Locate every Plasmodium parasite.
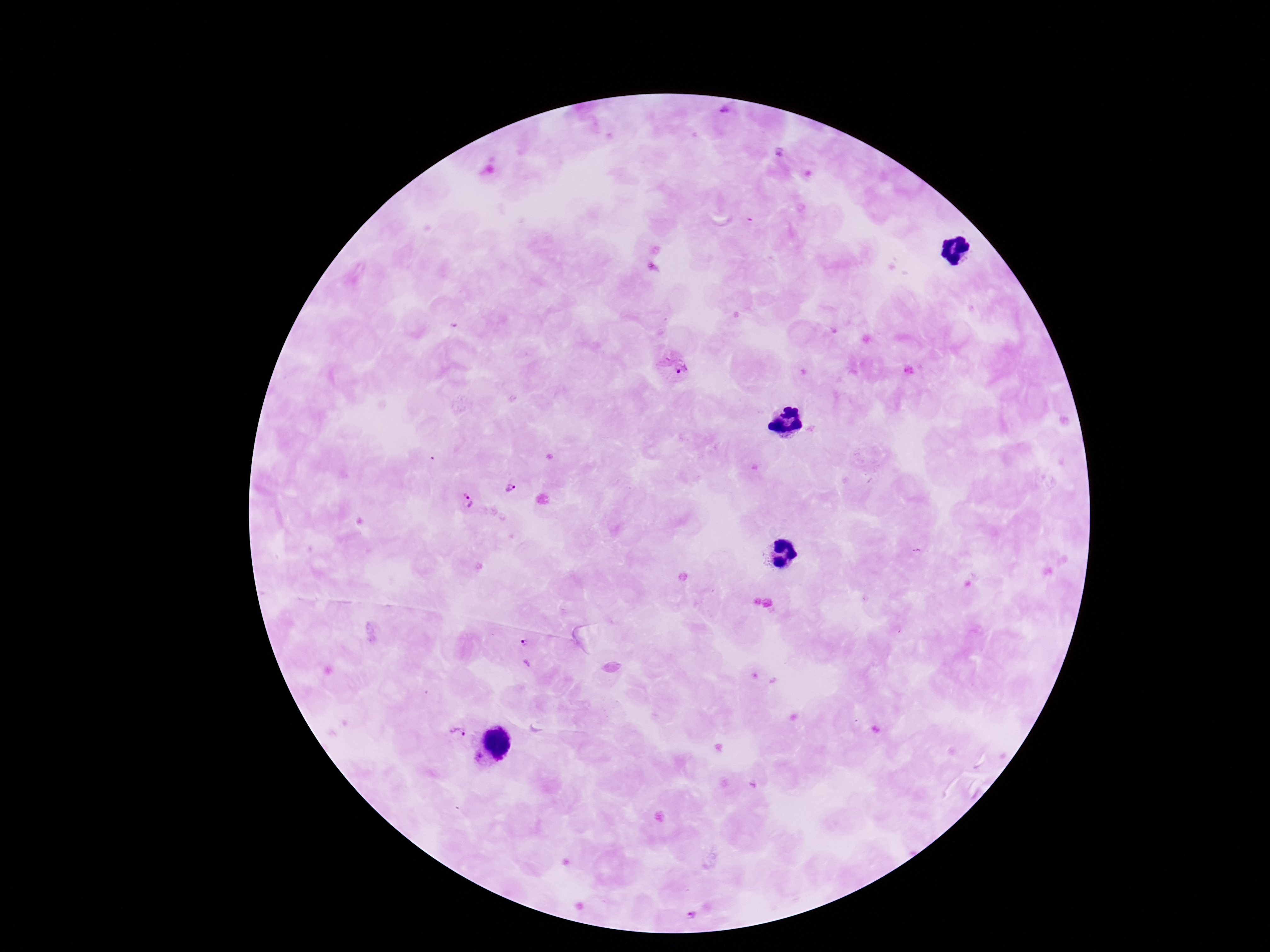
Approximate centers as [x, y] in pixels.
Plasmodium parasites: [726, 114], [671, 365], [512, 488], [467, 501], [526, 654], [457, 733], [689, 913].

Giemsa-stained preparation. Patient malaria status: positive. Single field of view. Smartphone photograph taken through the microscope eyepiece. Image is 1270×952 pixels. 100x magnification. Thick peripheral-blood smear.